Name the parasite shown.
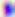

This is Toxoplasma gondii.

400x magnification. Micrograph.